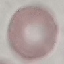
Summary:
  - Malaria status: uninfected
  - Stain: Giemsa
  - Image type: automatically extracted cell patch, resized to 64 × 64 pixels
  - Capture: smartphone camera at the microscope eyepiece
  - Preparation: thin blood film